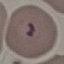
result = malaria parasites identified
capture = smartphone camera at the microscope eyepiece
image type = automatically extracted cell patch, resized to 64 × 64 pixels
stain = Giemsa
preparation = thin blood smear